Give the preparation type.
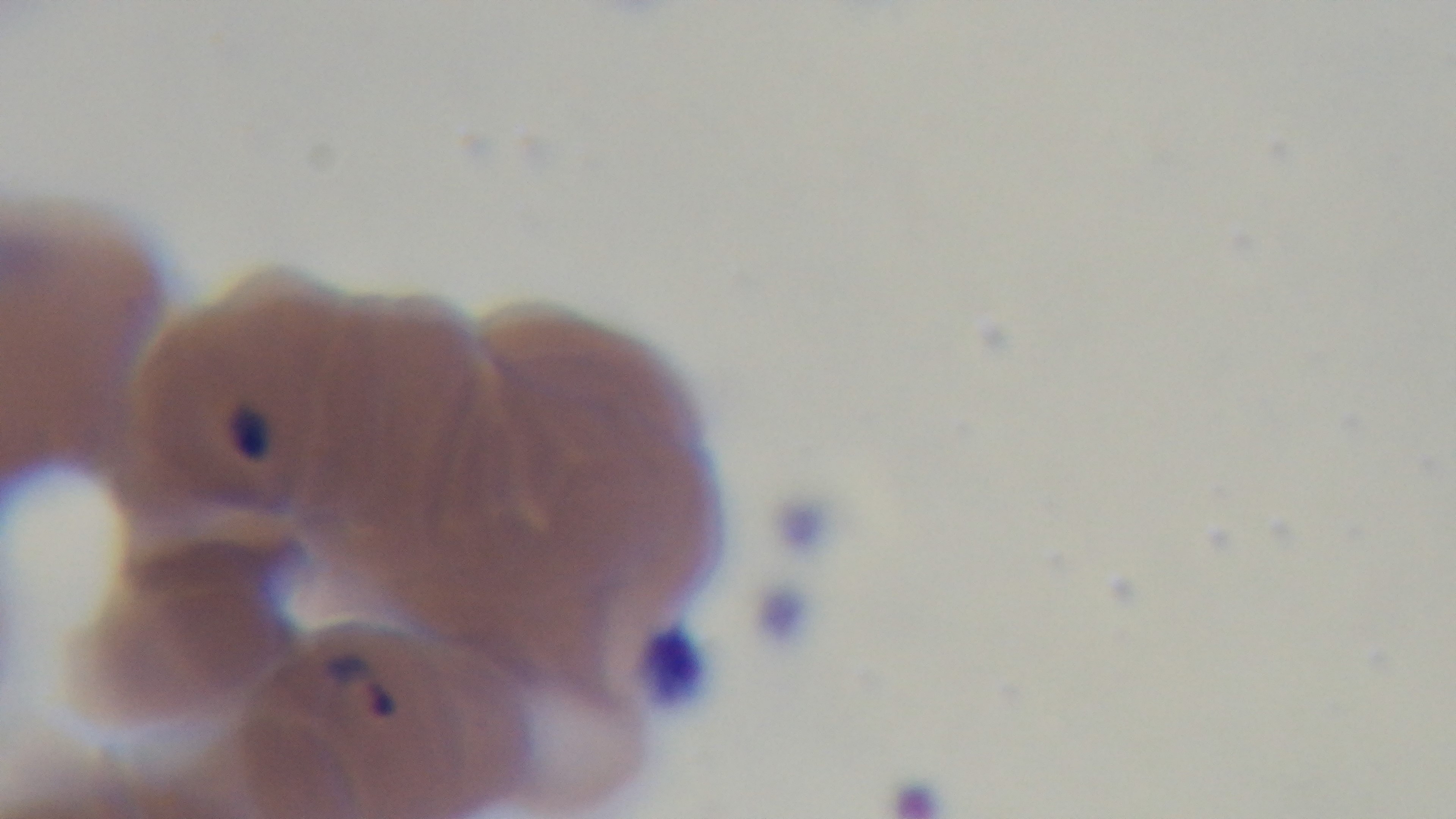
Thin.

Summary:
  - Capture: mounted 4K digital camera
  - Field of view: single
  - Stain: Giemsa
  - Malaria status: positive
  - Modality: light microscopy
  - Objective: 100x oil immersion